Classify this cell by malaria status.
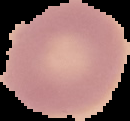
Uninfected.

Summary:
  - Preparation: thin blood smear
  - Image size: 130×121 pixels
  - Image type: segmented cell region on a black background